Outline each blood parasite and name the species.
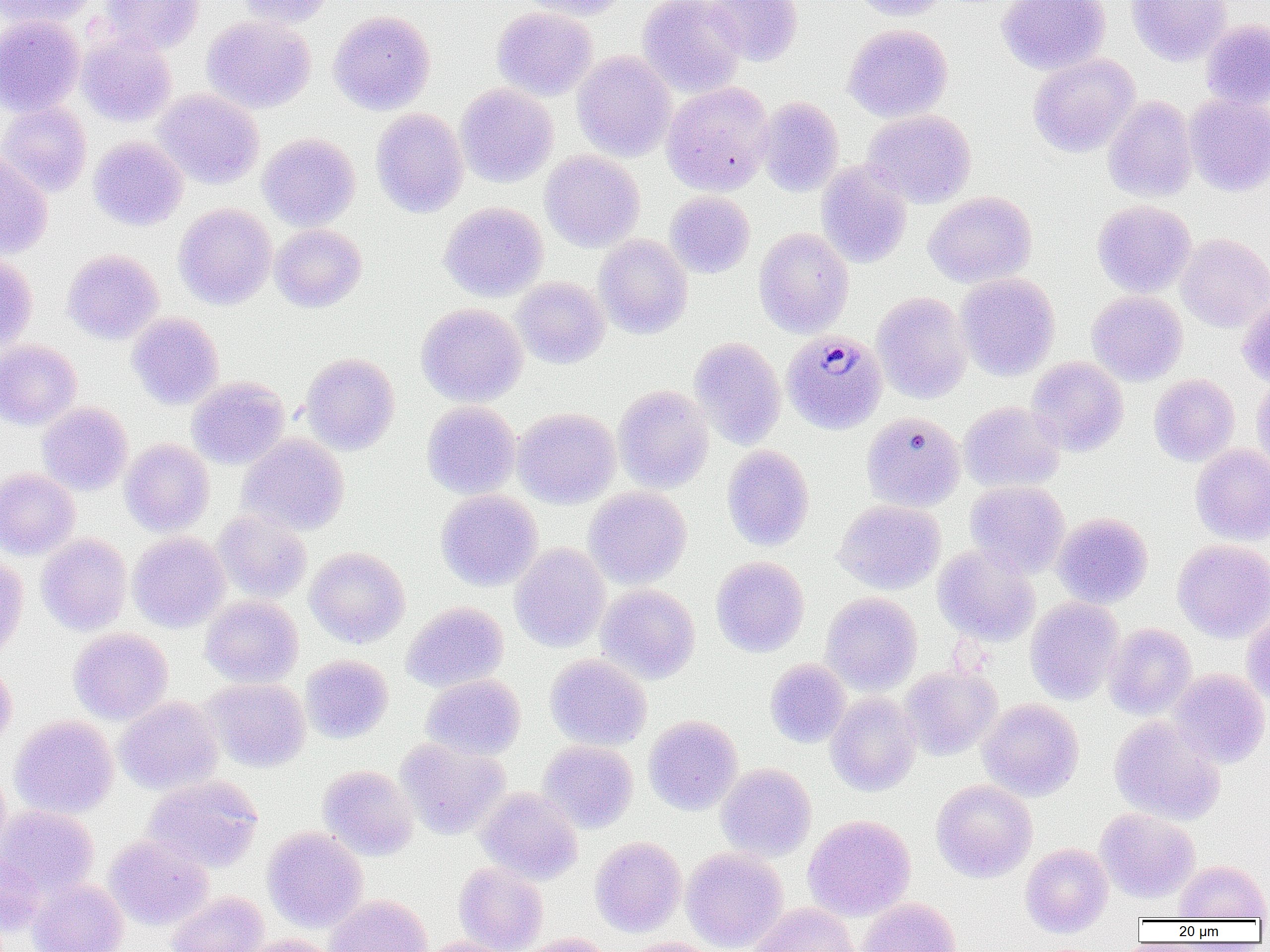

Approximate bounding boxes as (x1,y1)-(x2,y2) corner pairs in pixels.
Plasmodium malariae-infected red blood cells: (782,330)-(887,434).
No Plasmodium falciparum, Plasmodium ovale, Plasmodium vivax, Babesia divergens, or Trypanosoma brucei observed.

Summary:
  - Uninfected red blood cell locations: (2,0)-(97,29), (102,0)-(205,54), (235,0)-(334,28), (516,0)-(631,21), (638,0)-(747,97), (704,0)-(803,66), (849,0)-(950,20), (996,0)-(1110,76), (1127,0)-(1232,65), (491,6)-(597,101), (328,10)-(436,115), (0,14)-(85,116), (202,15)-(316,114), (1201,19)-(1270,109), (844,23)-(953,123), (77,32)-(177,127), (572,50)-(676,162), (1027,53)-(1140,157), (661,81)-(774,196), (455,83)-(558,188), (153,89)-(264,189), (1184,94)-(1270,196), (756,96)-(844,197), (1103,96)-(1198,202), (0,101)-(92,198), (370,107)-(469,218), (863,110)-(977,209), (258,132)-(361,231), (88,136)-(188,231), (540,150)-(645,252), (0,151)-(53,259), (816,161)-(913,269), (665,191)-(755,278), (923,191)-(1037,289), (1092,200)-(1197,298), (439,202)-(549,302), (173,203)-(277,309), (270,224)-(367,313), (753,227)-(854,338), (1176,233)-(1270,332), (594,234)-(693,339), (61,249)-(163,344), (0,254)-(38,352), (955,272)-(1060,381), (512,277)-(610,369), (873,291)-(972,404), (1087,291)-(1187,386), (1237,292)-(1270,386), (416,303)-(528,407), (127,312)-(224,410), (689,336)-(787,450), (0,340)-(82,430), (300,352)-(400,455), (1027,357)-(1128,456), (1251,373)-(1270,475), (1149,374)-(1240,466), (187,376)-(290,469), (613,384)-(714,493), (422,401)-(521,499), (958,401)-(1065,493), (37,402)-(133,495), (513,407)-(620,508), (862,412)-(965,511), (237,433)-(349,536), (120,438)-(215,536), (1190,444)-(1270,545), (721,445)-(815,551), (0,468)-(80,559), (965,481)-(1070,577), (584,486)-(691,589), (436,490)-(542,591), (833,500)-(945,594), (213,510)-(312,604), (1052,512)-(1152,608), (128,532)-(230,633), (36,534)-(132,635), (1172,539)-(1270,642), (510,543)-(611,652), (932,545)-(1040,646), (306,546)-(410,648), (711,556)-(809,657), (0,557)-(28,659), (595,584)-(700,684), (821,592)-(922,695), (201,595)-(303,688), (1025,597)-(1124,705), (402,601)-(509,692), (1242,613)-(1270,705), (1103,623)-(1196,720), (68,628)-(173,724), (301,654)-(393,743), (545,654)-(652,751), (0,659)-(17,751), (765,659)-(851,748), (899,665)-(1002,761), (1168,668)-(1270,768), (421,674)-(525,761), (201,678)-(311,773), (826,692)-(921,796), (114,696)-(222,795), (977,698)-(1084,801), (643,715)-(743,815), (10,716)-(118,819), (1109,716)-(1226,825), (395,738)-(510,839), (538,740)-(638,833), (716,763)-(816,861), (318,765)-(418,861), (0,767)-(12,866), (143,775)-(264,873), (931,779)-(1037,882), (476,786)-(583,884), (0,805)-(99,897), (1095,807)-(1200,903), (803,815)-(916,921), (262,827)-(367,932), (104,834)-(213,929), (590,837)-(687,937), (1020,842)-(1114,937), (681,847)-(788,952), (0,852)-(45,938), (1175,859)-(1270,921), (454,862)-(548,952), (28,878)-(129,952), (168,891)-(269,952), (323,895)-(432,952), (857,897)-(961,952), (749,903)-(859,952), (242,934)-(340,952), (513,934)-(616,952), (420,937)-(518,952), (616,937)-(723,952)
  - Slide-level diagnosis: Plasmodium malariae
  - Image size: 1270×952 pixels
  - Modality: optical microscopy
  - Field of view: one of a larger specimen
  - Preparation: thin blood smear
  - Magnification: 1000x